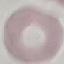

Malaria status: uninfected. Thin smear of blood. Acquired by smartphone through the microscope eyepiece. Automatically extracted cell patch, resized to 64 × 64 pixels. Giemsa stain.